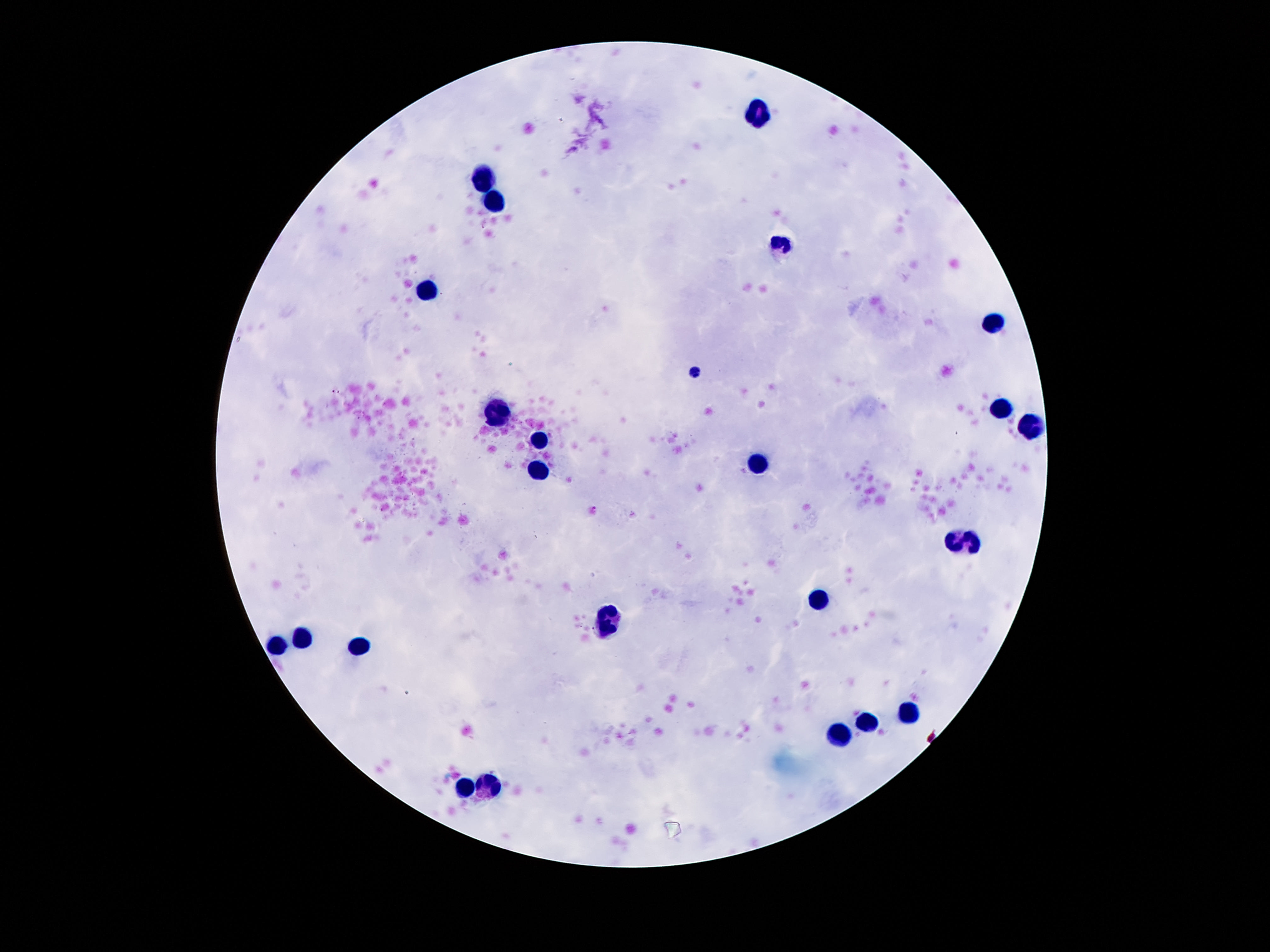

capture = smartphone camera through the microscope eyepiece
image size = 1270×952 pixels
patient malaria status = uninfected
field of view = single
leukocyte locations = approximate object centers, in pixels from the top-left corner: (x=761, y=113), (x=482, y=178), (x=490, y=199), (x=781, y=250), (x=425, y=289), (x=994, y=324), (x=998, y=408), (x=492, y=412), (x=1031, y=424), (x=542, y=440), (x=757, y=461), (x=540, y=468), (x=964, y=539), (x=820, y=600), (x=611, y=620), (x=302, y=633), (x=279, y=645), (x=357, y=649), (x=908, y=714), (x=869, y=722), (x=841, y=733), (x=470, y=784), (x=490, y=784)
preparation = thick blood smear
stain = Giemsa
magnification = 100x